Comment on the morphology of the red blood cells.
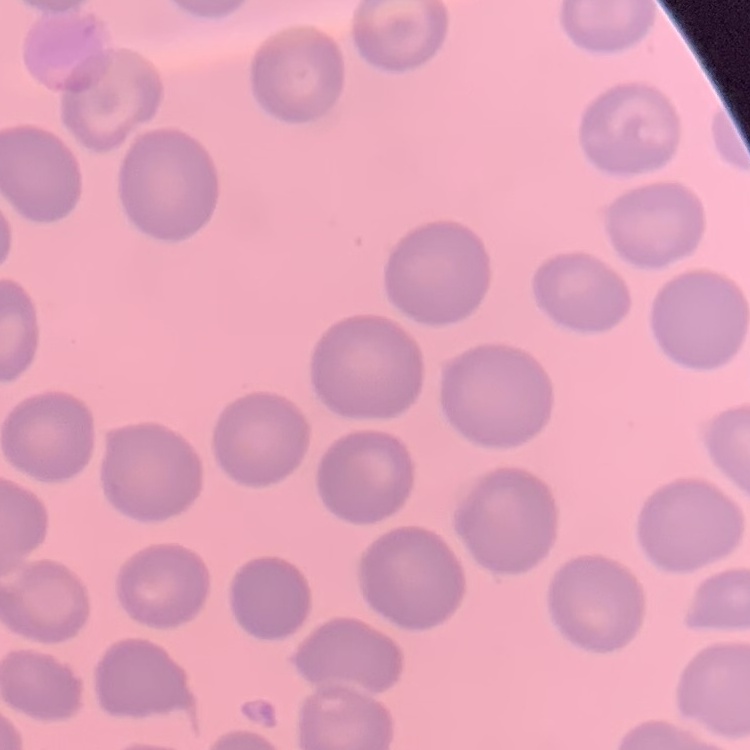
No rouleaux formation.

Summary:
  - Preparation: thin peripheral smear
  - Image type: one tile cut from a larger photomicrograph
  - Stain: Field's or Giemsa